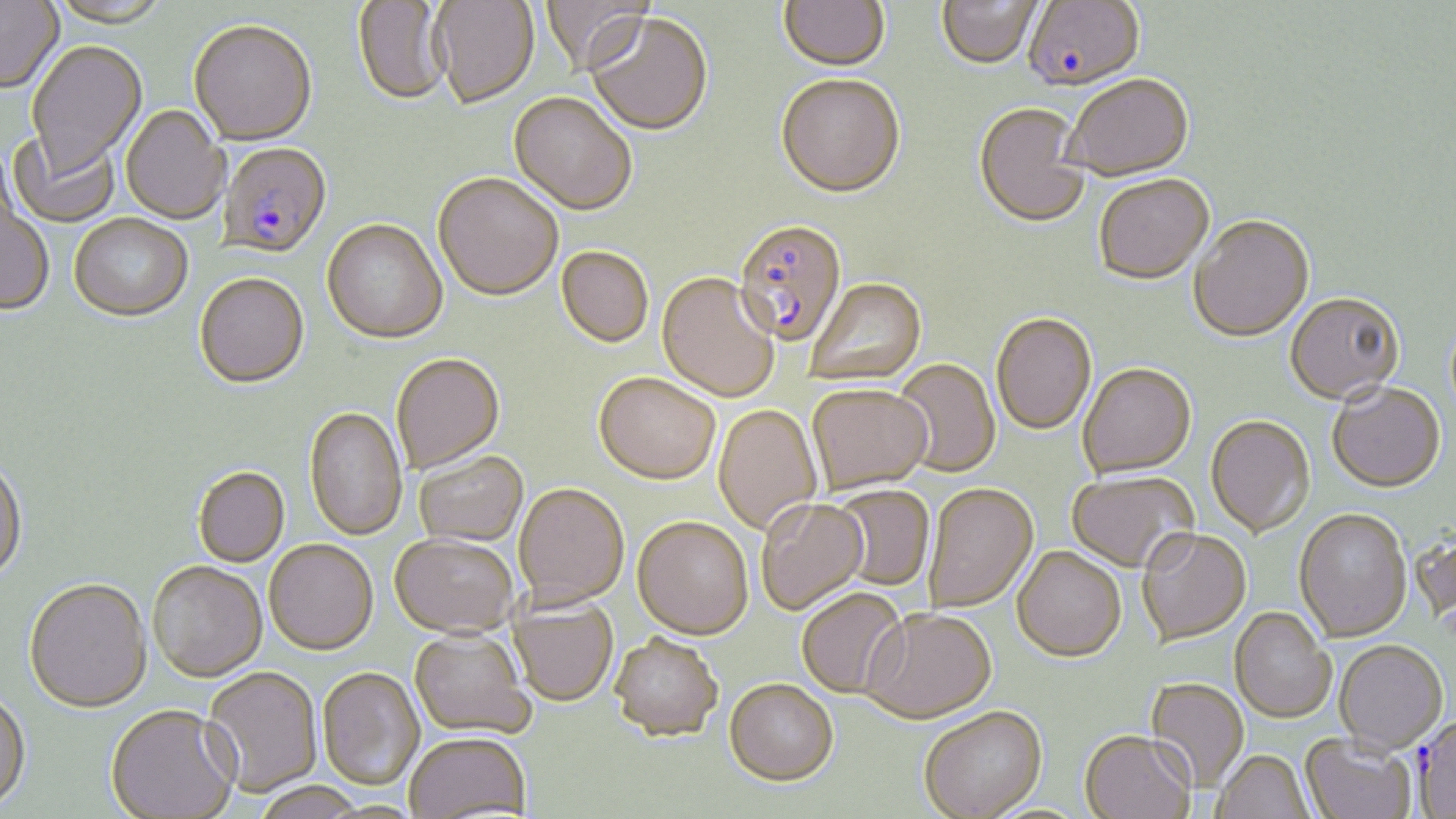

Approximate bounding boxes as (x1,y1)-(x2,y2) corner pairs in pixels. Uninfected red blood cell locations: (539,0)-(652,77), (778,0)-(891,74), (0,1)-(64,95), (47,1)-(170,30), (353,1)-(451,107), (432,1)-(539,111), (936,1)-(1042,71), (586,13)-(712,138), (188,23)-(317,148), (26,42)-(147,180), (1065,75)-(1194,182), (775,77)-(905,201), (509,93)-(637,218), (973,104)-(1091,230), (120,106)-(229,225), (7,131)-(119,229), (433,175)-(562,303), (1093,175)-(1214,285), (0,196)-(55,317), (69,214)-(193,323), (1189,216)-(1315,343), (322,221)-(448,346), (556,248)-(654,348), (657,273)-(779,402), (194,274)-(310,390), (806,278)-(927,387), (1285,291)-(1405,404), (991,313)-(1097,435), (391,355)-(505,475), (892,358)-(1001,478), (1078,363)-(1196,478), (593,373)-(720,485), (1327,382)-(1446,491), (807,383)-(932,495), (713,405)-(822,535), (304,408)-(407,542), (1206,415)-(1315,537), (414,453)-(528,548), (0,460)-(28,584), (193,467)-(290,567), (1066,469)-(1198,572), (924,482)-(1038,612), (514,484)-(629,608), (829,485)-(934,591), (756,498)-(869,615), (1294,507)-(1412,641), (632,517)-(753,641), (1137,527)-(1251,645), (390,535)-(519,639), (264,540)-(379,656), (1012,546)-(1127,662), (147,562)-(267,683), (24,581)-(153,715), (796,587)-(907,698), (508,597)-(618,707), (1230,606)-(1335,723), (861,607)-(997,723), (409,629)-(533,739), (610,635)-(723,743), (1334,639)-(1447,752), (202,667)-(322,798), (316,668)-(424,791), (1145,678)-(1249,792), (724,680)-(838,787), (0,692)-(31,814), (105,706)-(239,819), (919,706)-(1047,819), (1080,729)-(1196,819), (1301,733)-(1416,819), (404,734)-(531,818), (1212,750)-(1314,819), (252,784)-(367,818). Plasmodium falciparum-infected red blood cell locations: (1023,1)-(1143,93), (219,144)-(332,260), (733,219)-(848,348). Slide-level diagnosis: Plasmodium falciparum. Optical microscopy. Thin blood film. Captured at 1000x magnification. Image is 1456×819 pixels. Single field of view. May-Grünwald-Giemsa-stained preparation.